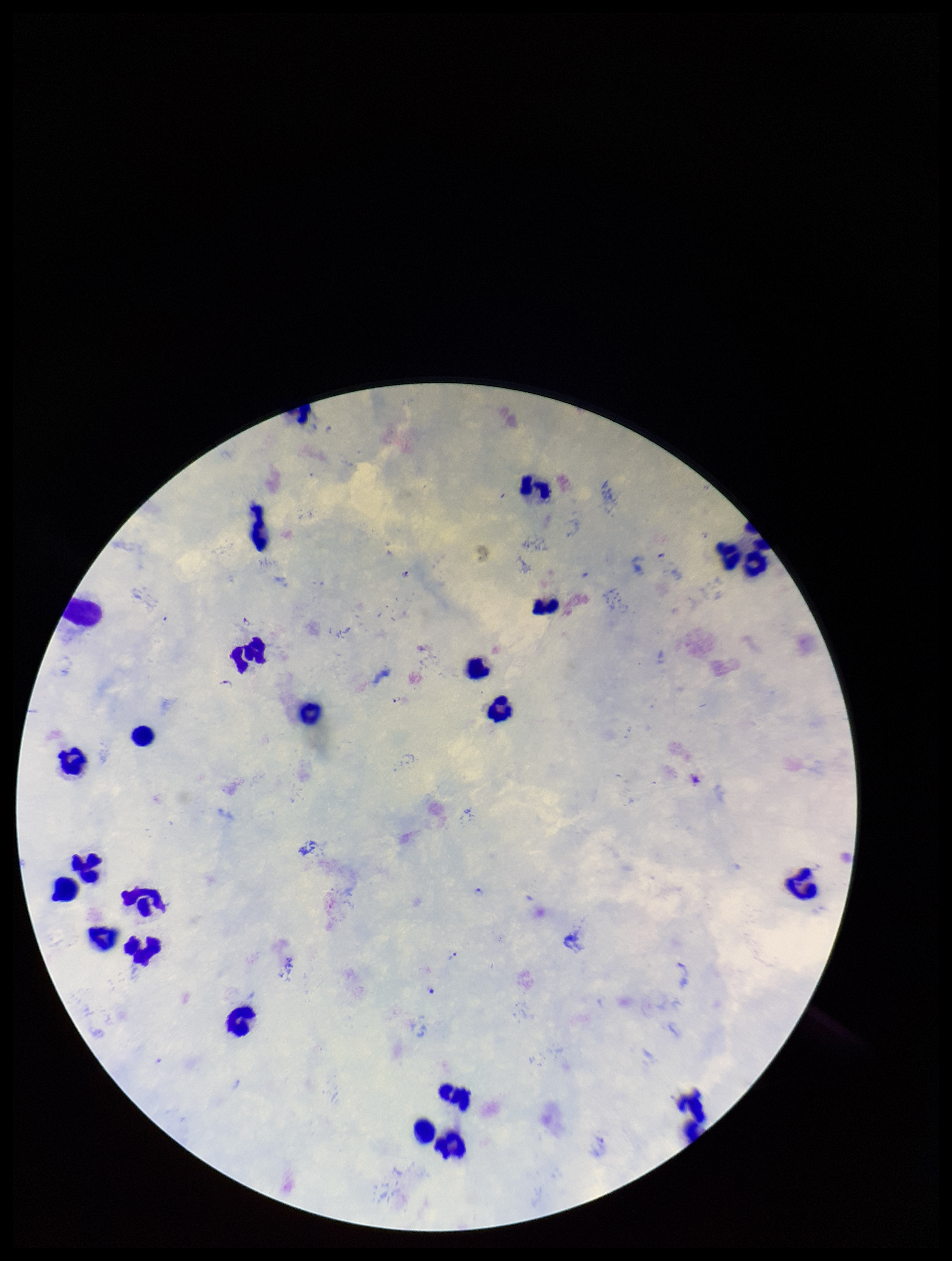
Summary:
  - Patient malaria status: infected
  - Parasite count: 4
  - Image size: 952×1261 pixels
  - Capture: smartphone photograph through the microscope eyepiece
  - Plasmodium parasites: seen
  - Field of view: single
  - Species reported for this patient: Plasmodium falciparum
  - Leukocyte count: 23
  - Stain: Giemsa
  - Preparation: thick smear